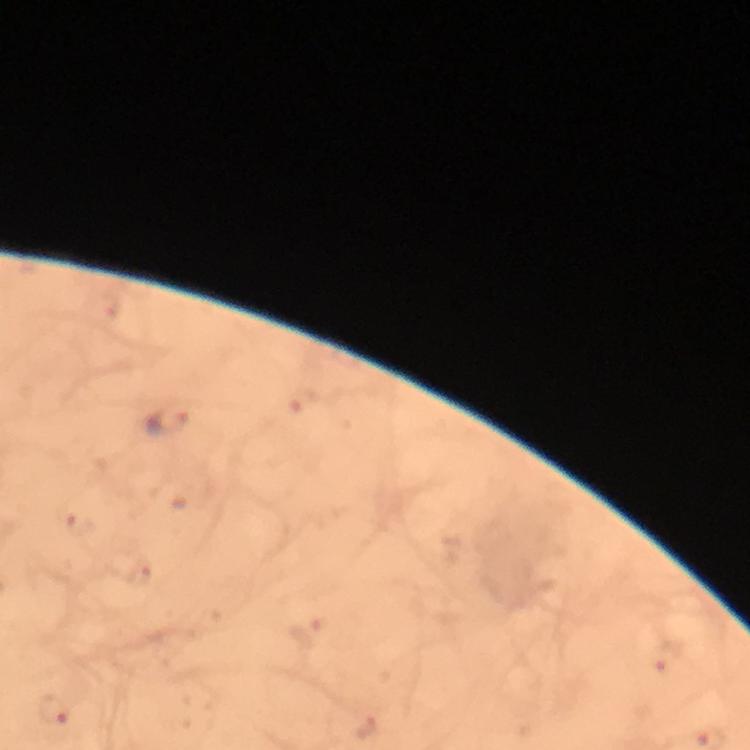
Approximate centers as [x, y] in pixels.
Summary:
  - Plasmodium parasite locations: [167, 424]
  - Capture: smartphone camera through the microscope
  - Magnification: 100x
  - Stain: Giemsa
  - Preparation: thick smear
  - Image size: 750×750 pixels
  - Immersion oil: used
  - Context: from a diagnostic examination for malaria
  - Cropped from: a single field of view